Assess this cell for malaria.
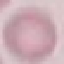
It is uninfected.

image_type: cell patch, automatically extracted from a larger field of view and resized to 64 × 64 pixels
capture: smartphone camera at the microscope eyepiece
preparation: thin blood smear
stain: Giemsa